Classify this cell by malaria status.
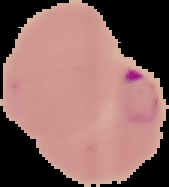
It is parasitized.

Image is 169×187 pixels. From a thin blood smear. Cell region segmented out of the field of view; the surrounding area is masked to black.